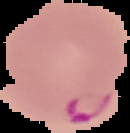
Summary:
  - Malaria status: parasitized
  - Image size: 130×133 pixels
  - Preparation: thin blood smear
  - Image type: segmented cell region with the area outside set to black